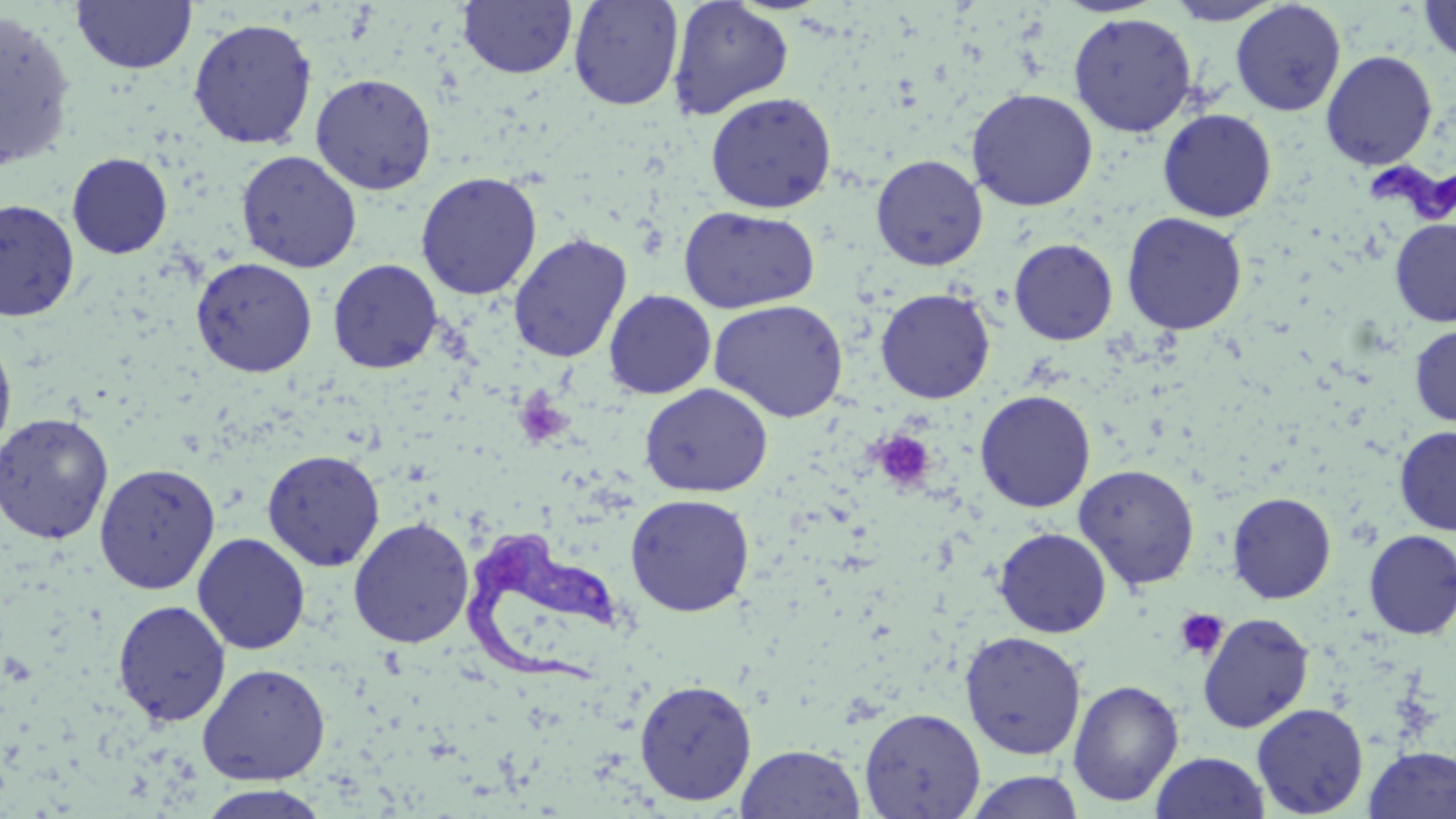

slide-level diagnosis = Trypanosoma brucei
field of view = one of a larger specimen
uninfected red blood cell locations = approximate bounding boxes as (x1, y1, x2, y2) in pixels: (71, 0, 197, 74), (667, 0, 794, 120), (1165, 0, 1285, 26), (1418, 0, 1456, 63), (457, 1, 578, 79), (568, 1, 684, 111), (1229, 1, 1346, 116), (0, 9, 77, 172), (1067, 12, 1198, 137), (187, 17, 318, 150), (1320, 50, 1438, 170), (310, 72, 437, 195), (966, 88, 1098, 211), (705, 91, 837, 214), (1157, 108, 1277, 222), (236, 150, 362, 272), (67, 152, 173, 259), (871, 154, 988, 271), (415, 171, 543, 300), (0, 198, 80, 322), (678, 206, 820, 314), (1121, 211, 1248, 335), (1390, 218, 1456, 326), (508, 233, 632, 363), (1009, 238, 1118, 345), (191, 257, 317, 377), (327, 258, 443, 374), (875, 288, 995, 404), (604, 289, 716, 399), (709, 299, 848, 422), (1409, 325, 1456, 426), (0, 331, 17, 456), (639, 383, 773, 498), (975, 390, 1096, 513), (1, 412, 114, 545), (1394, 425, 1456, 535), (262, 449, 385, 571), (94, 462, 221, 595), (1074, 463, 1200, 590), (1227, 491, 1336, 604), (625, 493, 755, 617), (348, 517, 475, 648), (994, 527, 1111, 638), (1363, 530, 1456, 639), (192, 532, 311, 655), (112, 599, 232, 727), (1197, 612, 1315, 733), (959, 631, 1087, 760), (197, 663, 331, 784), (634, 679, 758, 805), (1068, 679, 1183, 806), (1251, 703, 1369, 817), (859, 706, 985, 818), (736, 743, 866, 818), (1363, 746, 1456, 819), (1149, 751, 1271, 818), (964, 770, 1083, 818), (195, 784, 334, 818)
preparation = thin blood film
platelet locations = approximate bounding boxes as (x1, y1, x2, y2) in pixels: (513, 390, 572, 447), (873, 431, 936, 492), (1173, 608, 1228, 661)
modality = optical microscopy
image size = 1456×819 pixels
Trypanosoma brucei locations = approximate bounding boxes as (x1, y1, x2, y2) in pixels: (1368, 148, 1455, 226), (459, 527, 624, 690)
stain = May-Grünwald-Giemsa
magnification = 1000x